Point out each Plasmodium parasite.
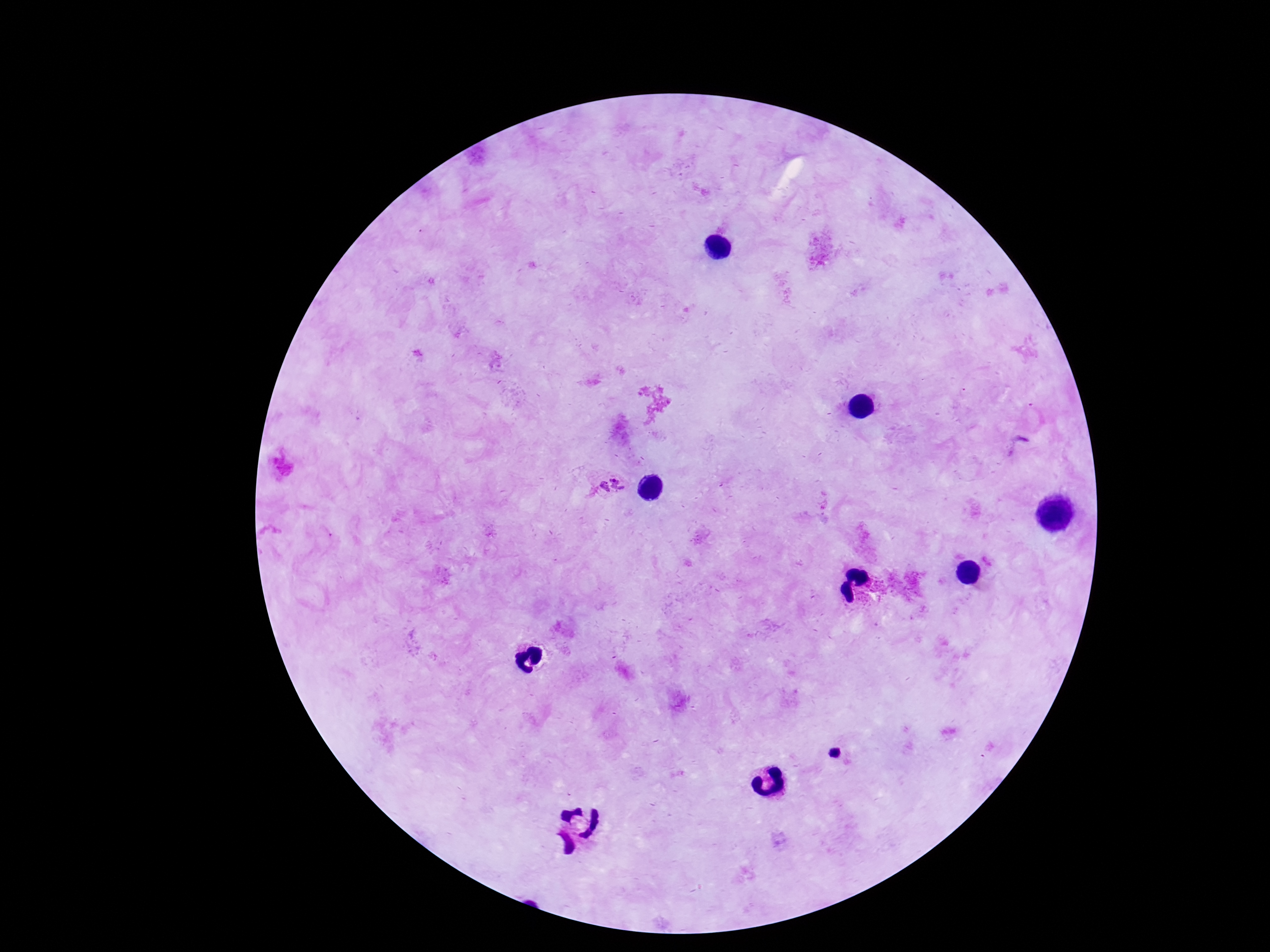

Approximate object centers, in pixels from the top-left corner.
Plasmodium parasites: (x=611, y=485), (x=834, y=755).

Summary:
  - Stain: Giemsa
  - Preparation: thick blood smear
  - Image size: 1270×952 pixels
  - Capture: smartphone camera through the microscope eyepiece
  - Field of view: single
  - Patient malaria status: infected
  - Magnification: 100x